Outline each uninfected red blood cell.
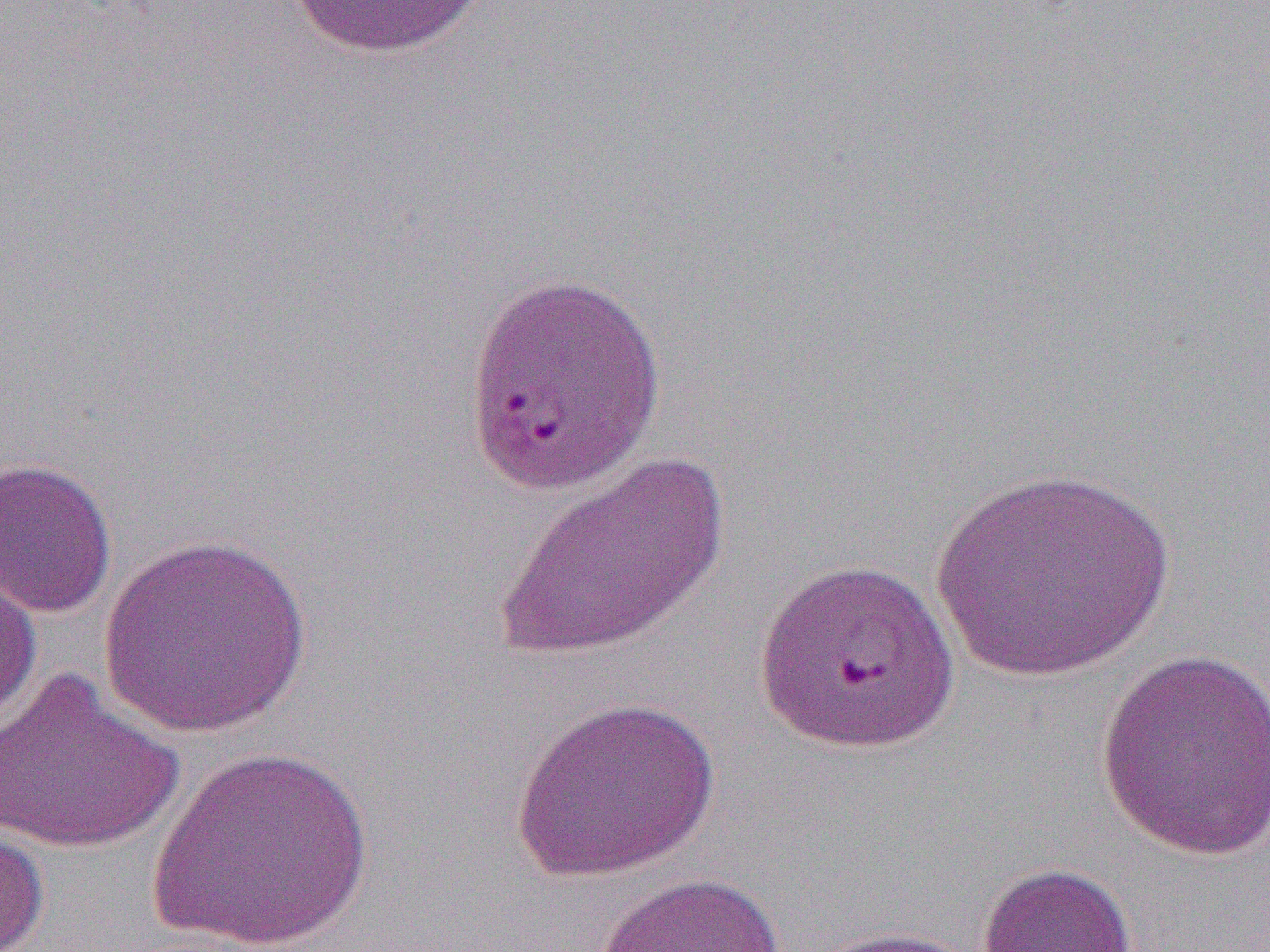

Approximate bounding boxes as (x1,y1)-(x2,y2) corner pairs in pixels.
Uninfected red blood cells: (284,1)-(491,60), (461,265)-(665,498), (497,449)-(732,661), (0,456)-(118,617), (932,465)-(1176,683), (95,533)-(315,738), (0,562)-(43,732), (1094,646)-(1270,860), (1,669)-(184,856), (508,693)-(722,883), (150,745)-(373,952), (0,819)-(49,952), (975,861)-(1139,952), (589,870)-(789,952), (803,925)-(989,952).

slide-level diagnosis = Plasmodium falciparum
modality = light microscopy
magnification = 1000x
preparation = thin blood smear
field of view = one of a larger specimen
image size = 1270×952 pixels